Report the malaria status of this cell.
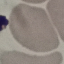
Uninfected.

Automatically extracted cell patch, resized to 64 × 64 pixels. Giemsa stain. Acquired by smartphone through the microscope eyepiece. Thin smear of blood.